Name the parasite shown.
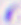
This is Toxoplasma gondii.

Micrograph. 400x magnification.